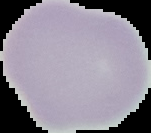
Summary:
  - Image size: 151×133 pixels
  - Image type: segmented cell region on a black background
  - Preparation: thin blood smear
  - Result: negative for Plasmodium parasites